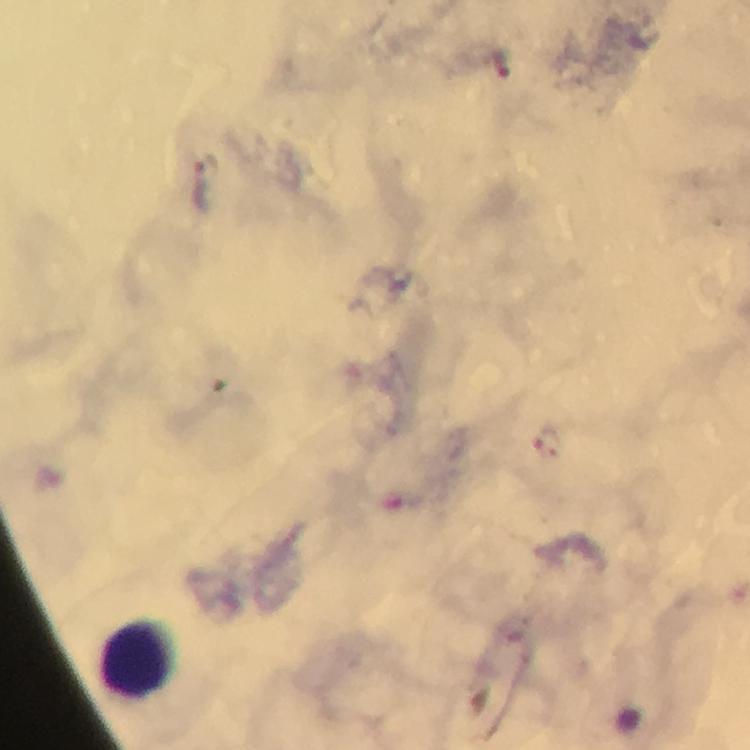

magnification: 100x
preparation: thick blood film
capture: smartphone camera through the microscope
cropped_from: a single field of view
leukocyte_locations: 'approximate centers as {x, y} in pixels: {139, 657}'
stain: Giemsa
malaria_parasite_locations: 'approximate centers as {x, y} in pixels: {200, 190}'
image_size: 750×750 pixels
context: from a malaria diagnostic workup
immersion_oil: used